Assess the morphology of the red blood cells.
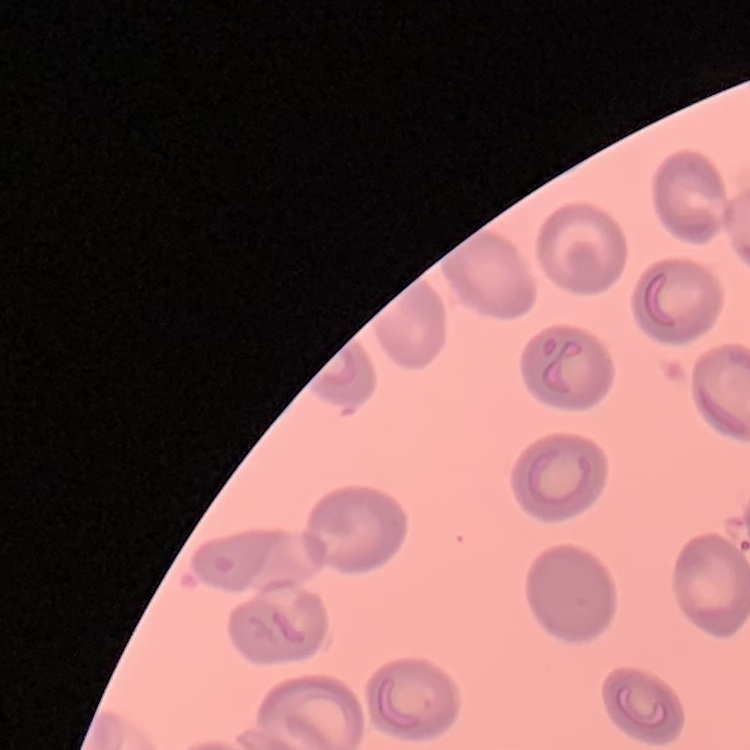

They show no rouleaux formation.

Summary:
  - Stain: Field's or Giemsa
  - Image type: square crop of a larger photomicrograph
  - Preparation: thin blood film